Outline each blood parasite and name the species.
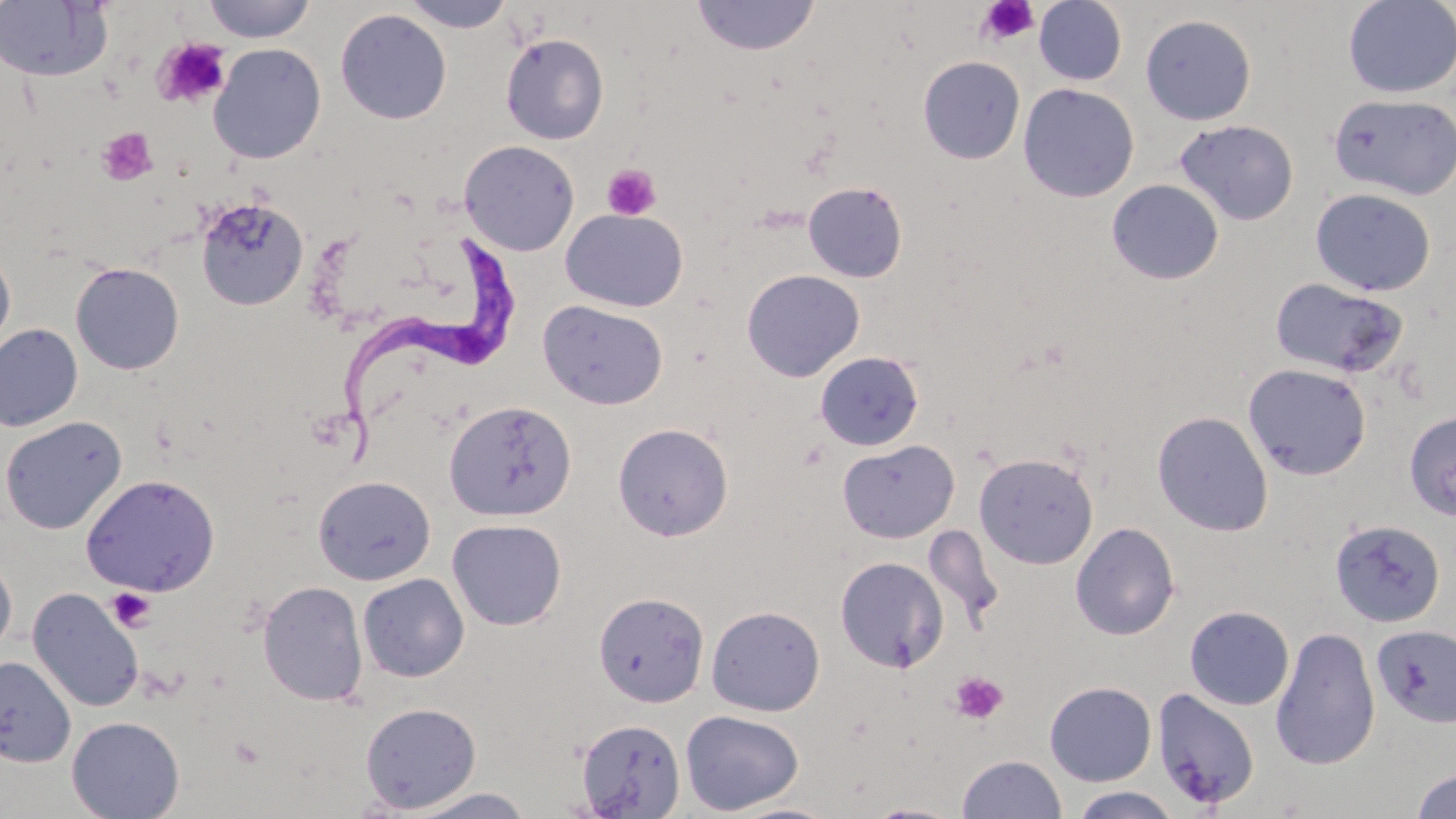
Approximate bounding boxes as (x1, y1, x2, y2) in pixels.
Trypanosoma brucei: (343, 230, 525, 466).
No Plasmodium falciparum, Plasmodium ovale, Plasmodium malariae, Plasmodium vivax, or Babesia divergens observed.

Platelet locations: (976, 0, 1040, 45), (152, 38, 230, 109), (96, 126, 159, 187), (601, 163, 662, 221), (106, 587, 156, 633), (948, 671, 1008, 725). Uninfected red blood cell locations: (201, 0, 318, 43), (400, 0, 516, 33), (691, 0, 820, 56), (1033, 0, 1128, 86), (1343, 1, 1456, 98), (0, 2, 112, 82), (335, 9, 452, 125), (1140, 13, 1257, 125), (500, 33, 609, 145), (208, 43, 327, 165), (918, 56, 1025, 164), (1018, 83, 1139, 203), (1329, 93, 1456, 200), (1174, 119, 1299, 226), (459, 140, 580, 255), (1106, 179, 1224, 285), (802, 181, 908, 283), (1310, 188, 1436, 296), (195, 196, 309, 311), (561, 208, 688, 312), (0, 244, 16, 353), (70, 262, 184, 375), (741, 269, 865, 382), (1269, 277, 1409, 377), (538, 299, 668, 410), (0, 324, 83, 432), (815, 351, 924, 451), (1243, 363, 1372, 481), (444, 399, 577, 522), (1152, 410, 1274, 536), (1404, 410, 1456, 521), (0, 415, 126, 535), (613, 423, 733, 541), (837, 439, 960, 543), (974, 453, 1099, 569), (81, 474, 220, 597), (313, 475, 436, 585), (447, 519, 567, 630), (1330, 519, 1445, 628), (1070, 522, 1180, 640), (0, 553, 17, 659), (835, 556, 949, 673), (358, 573, 470, 682), (257, 580, 368, 707), (27, 587, 144, 712), (593, 592, 709, 707), (706, 605, 825, 716), (1184, 605, 1294, 711), (1372, 624, 1456, 728), (1270, 626, 1381, 771), (0, 655, 76, 767), (1044, 681, 1156, 786), (1151, 688, 1261, 810), (360, 702, 482, 813), (680, 709, 804, 814), (66, 716, 185, 819), (575, 717, 686, 818), (957, 754, 1066, 818), (1410, 767, 1456, 819), (1069, 787, 1181, 818), (404, 788, 535, 819), (862, 801, 967, 819), (721, 802, 843, 819). Slide-level diagnosis: Trypanosoma brucei. Light microscopy. Captured at 1000x magnification. Image is 1456×819 pixels. May-Grünwald-Giemsa stain. Thin blood smear. One field of a larger specimen.